Outline each Trypanosoma brucei.
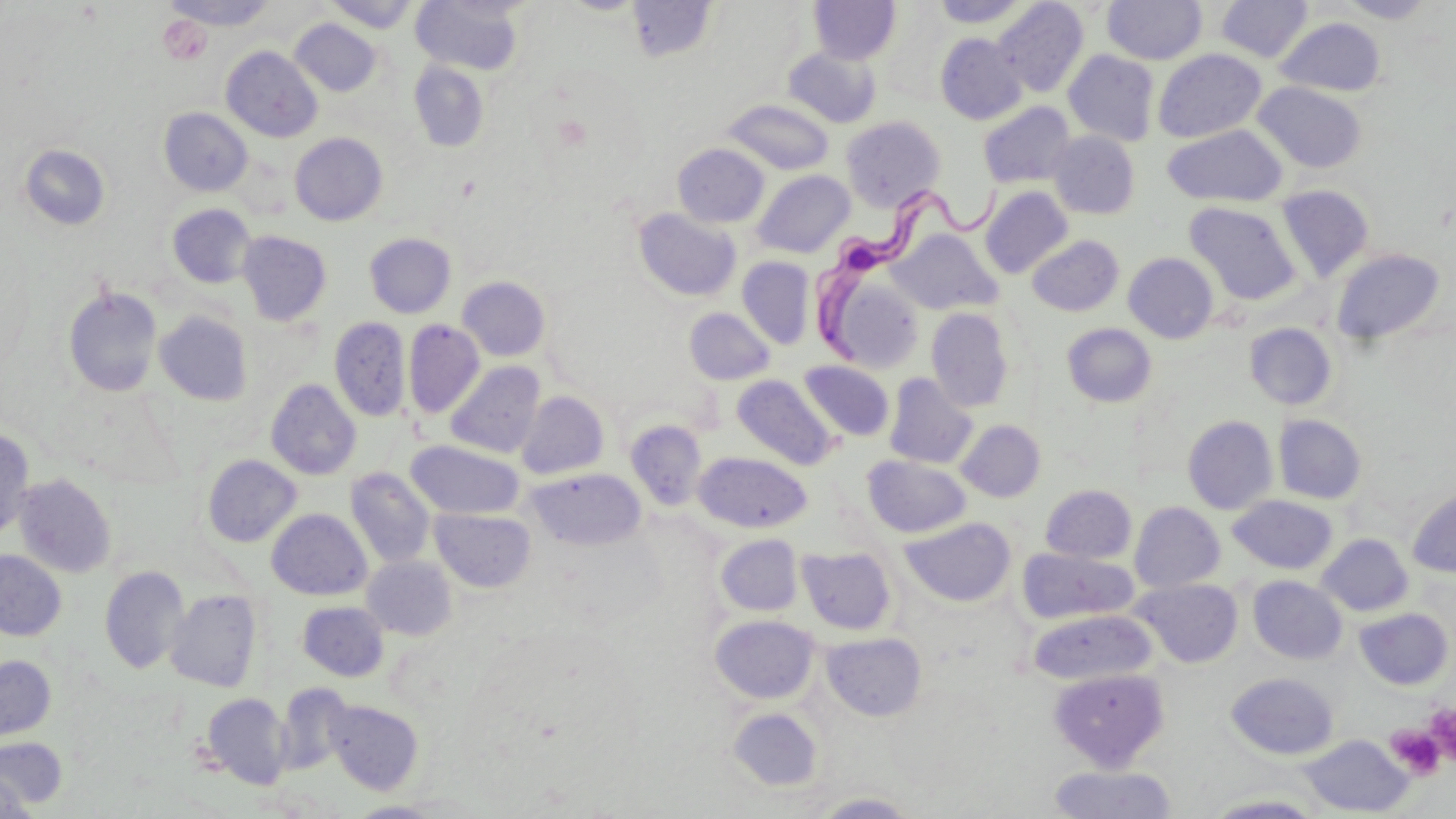

Approximate bounding boxes as (x1, y1, x2, y2) in pixels.
Trypanosoma brucei: (814, 179, 1022, 365).

slide-level diagnosis = Trypanosoma brucei
stain = May-Grünwald-Giemsa
preparation = thin blood smear
image size = 1456×819 pixels
modality = optical microscopy
uninfected red blood cell locations = approximate bounding boxes as (x1, y1, x2, y2) in pixels: (162, 0, 279, 30), (628, 0, 718, 63), (933, 0, 1030, 27), (1103, 0, 1207, 65), (1216, 0, 1313, 62), (1337, 0, 1438, 23), (325, 1, 419, 33), (411, 1, 525, 76), (809, 1, 900, 65), (993, 1, 1089, 96), (876, 8, 955, 102), (1276, 17, 1386, 97), (290, 19, 381, 96), (935, 33, 1027, 124), (222, 46, 323, 142), (783, 47, 880, 128), (1153, 48, 1266, 143), (1064, 50, 1160, 146), (408, 61, 489, 151), (1253, 82, 1367, 173), (721, 99, 834, 175), (978, 102, 1076, 188), (159, 107, 252, 196), (840, 116, 945, 211), (1163, 124, 1288, 206), (1047, 131, 1140, 219), (290, 132, 388, 226), (19, 143, 111, 231), (672, 143, 769, 228), (753, 170, 855, 257), (1276, 185, 1373, 283), (980, 186, 1073, 278), (1184, 201, 1301, 305), (167, 203, 257, 289), (632, 208, 741, 302), (889, 229, 1001, 314), (237, 230, 332, 326), (364, 232, 456, 319), (1028, 235, 1124, 316), (1332, 248, 1445, 345), (1124, 253, 1219, 343), (737, 257, 815, 349), (457, 276, 551, 361), (62, 285, 163, 398), (684, 307, 774, 385), (926, 308, 1014, 412), (154, 311, 253, 406), (329, 316, 411, 422), (403, 320, 484, 419), (1062, 323, 1157, 407), (1244, 323, 1337, 409), (799, 360, 894, 441), (446, 361, 545, 458), (884, 373, 978, 469), (731, 374, 837, 470), (266, 379, 362, 480), (516, 391, 609, 479), (1274, 414, 1367, 504), (1183, 415, 1278, 514), (625, 420, 708, 511), (956, 420, 1045, 502), (0, 427, 35, 542), (406, 440, 524, 520), (695, 452, 812, 532), (202, 454, 301, 548), (863, 455, 970, 537), (345, 467, 436, 568), (527, 469, 646, 550), (14, 474, 116, 578), (1040, 484, 1137, 564), (1407, 485, 1456, 577), (1228, 495, 1338, 575), (1129, 502, 1225, 592), (430, 507, 536, 593), (267, 509, 372, 600), (901, 517, 1016, 606), (716, 534, 803, 616), (1317, 534, 1413, 616), (797, 545, 897, 635), (1017, 548, 1138, 625), (0, 550, 66, 641), (362, 556, 457, 640), (99, 565, 189, 674), (1249, 575, 1347, 664), (1132, 578, 1242, 668), (166, 589, 262, 691), (297, 601, 389, 681), (1356, 608, 1453, 690), (1028, 609, 1156, 685), (709, 615, 819, 704), (822, 632, 927, 721), (0, 655, 55, 741), (1048, 667, 1169, 770), (1226, 672, 1338, 759), (275, 682, 354, 776), (202, 693, 291, 789), (325, 699, 423, 795), (727, 707, 823, 791), (1300, 734, 1413, 816), (0, 736, 67, 809), (1048, 763, 1178, 819), (0, 770, 34, 819), (812, 792, 919, 818), (1203, 793, 1329, 818)
platelet locations = approximate bounding boxes as (x1, y1, x2, y2) in pixels: (158, 16, 212, 66), (1429, 704, 1456, 766), (1387, 725, 1446, 780)
field of view = single
magnification = 1000x